Report the malaria status of this cell.
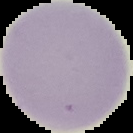
Uninfected.

{
  "image_type": "cell region segmented out of the field of view; surrounding area masked to black",
  "preparation": "thin blood film",
  "image_size": "133×133 pixels"
}